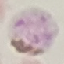

Summary:
  - Malaria status: parasitized
  - Image type: automatically extracted cell patch, resized to 64 × 64 pixels
  - Preparation: thin blood film
  - Stain: Giemsa
  - Capture: smartphone camera at the microscope eyepiece